Classify this cell by malaria status.
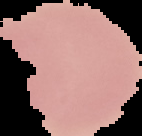

Uninfected.

image type = segmented cell region with the area outside set to black
image size = 142×136 pixels
preparation = thin blood smear